Assess this cell for malaria.
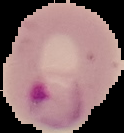
It is parasitized.

Segmented cell region on a black background. Image is 124×133 pixels. From a thin blood film.